Name the blood parasite species.
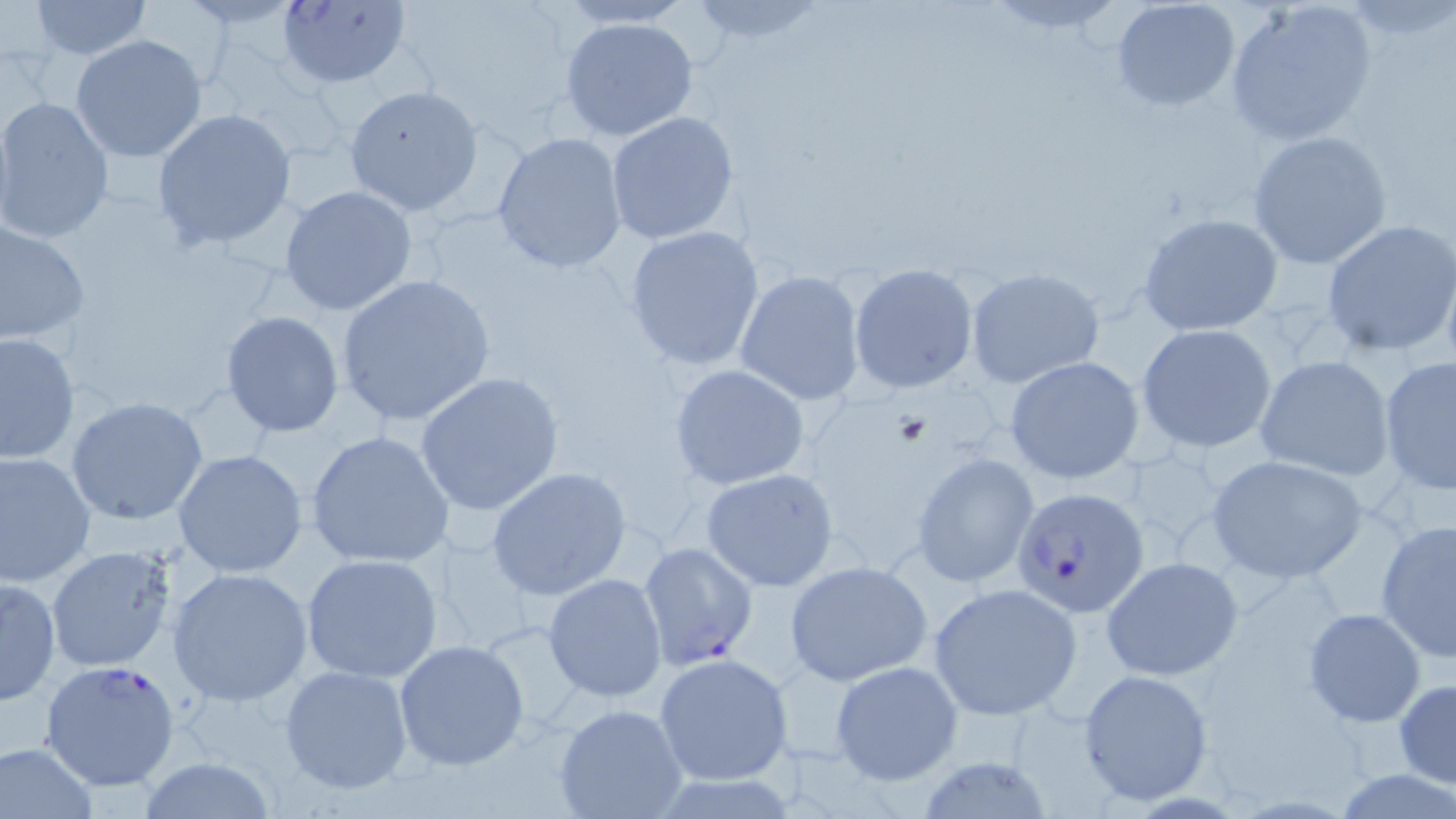
Plasmodium falciparum.

Approximate bounding boxes as [x1, y1, x2, y2] in pixels. Plasmodium falciparum-infected red blood cell locations: [280, 0, 410, 91], [1005, 487, 1143, 619], [639, 540, 758, 671], [40, 660, 184, 793]. Uninfected red blood cell locations: [27, 0, 154, 58], [1224, 0, 1380, 149], [553, 1, 698, 28], [680, 1, 832, 52], [1111, 1, 1241, 114], [557, 16, 701, 142], [69, 35, 206, 163], [344, 86, 484, 215], [0, 97, 113, 242], [149, 107, 298, 253], [605, 112, 741, 246], [492, 130, 627, 273], [1247, 130, 1393, 269], [279, 185, 419, 315], [1137, 211, 1284, 336], [1321, 219, 1456, 356], [0, 220, 91, 347], [622, 225, 767, 372], [849, 263, 979, 394], [966, 268, 1105, 390], [735, 269, 866, 406], [335, 274, 495, 425], [221, 311, 346, 436], [1136, 323, 1278, 454], [0, 330, 80, 465], [1255, 354, 1396, 483], [1005, 355, 1146, 486], [1378, 355, 1456, 494], [669, 364, 810, 489], [416, 371, 564, 519], [66, 396, 208, 525], [305, 430, 452, 569], [173, 449, 308, 579], [0, 450, 97, 588], [911, 451, 1040, 587], [1206, 454, 1368, 582], [486, 466, 631, 599], [701, 468, 841, 592], [1375, 519, 1455, 664], [42, 543, 182, 673], [300, 553, 443, 682], [1101, 556, 1243, 681], [784, 560, 933, 685], [167, 566, 314, 707], [543, 573, 668, 703], [1, 576, 61, 706], [928, 583, 1081, 718], [1303, 606, 1427, 727], [394, 640, 531, 771], [654, 653, 794, 787], [829, 661, 962, 786], [280, 664, 417, 796], [1078, 669, 1215, 805], [1394, 679, 1456, 790], [553, 703, 690, 819], [1, 740, 101, 818], [133, 757, 283, 817]. Captured at 1000x magnification. Thin blood smear. Image is 1456×819 pixels. May-Grünwald-Giemsa stain. One field of a larger specimen. Light microscopy.